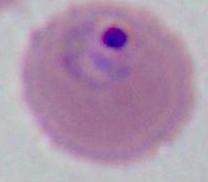
Captured at either 400x or 1000x magnification. A Plasmodium parasite is shown. Micrograph.